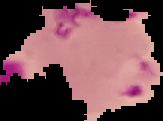 From a thin blood smear. Malaria status: parasitized. Segmented cell region on a black background. Image is 163×121 pixels.